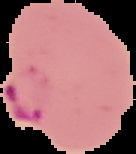

image size = 136×154 pixels
malaria status = parasitized
image type = segmented cell region on a black background
preparation = thin blood film